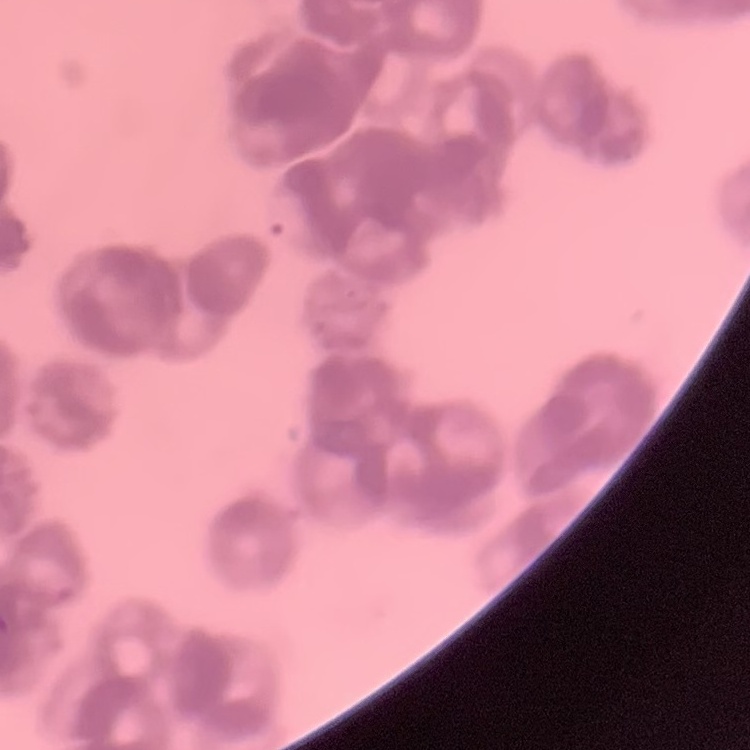

The red blood cells exhibit rouleaux formation. One tile cut from a larger photomicrograph. Thin blood smear. Field's or Giemsa stain.